Report the malaria status of this cell.
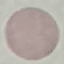

Uninfected.

Giemsa stain. Thin smear of blood. Cell patch, automatically extracted from a larger field of view and resized to 64 × 64 pixels. Photographed with a smartphone camera at the microscope eyepiece.